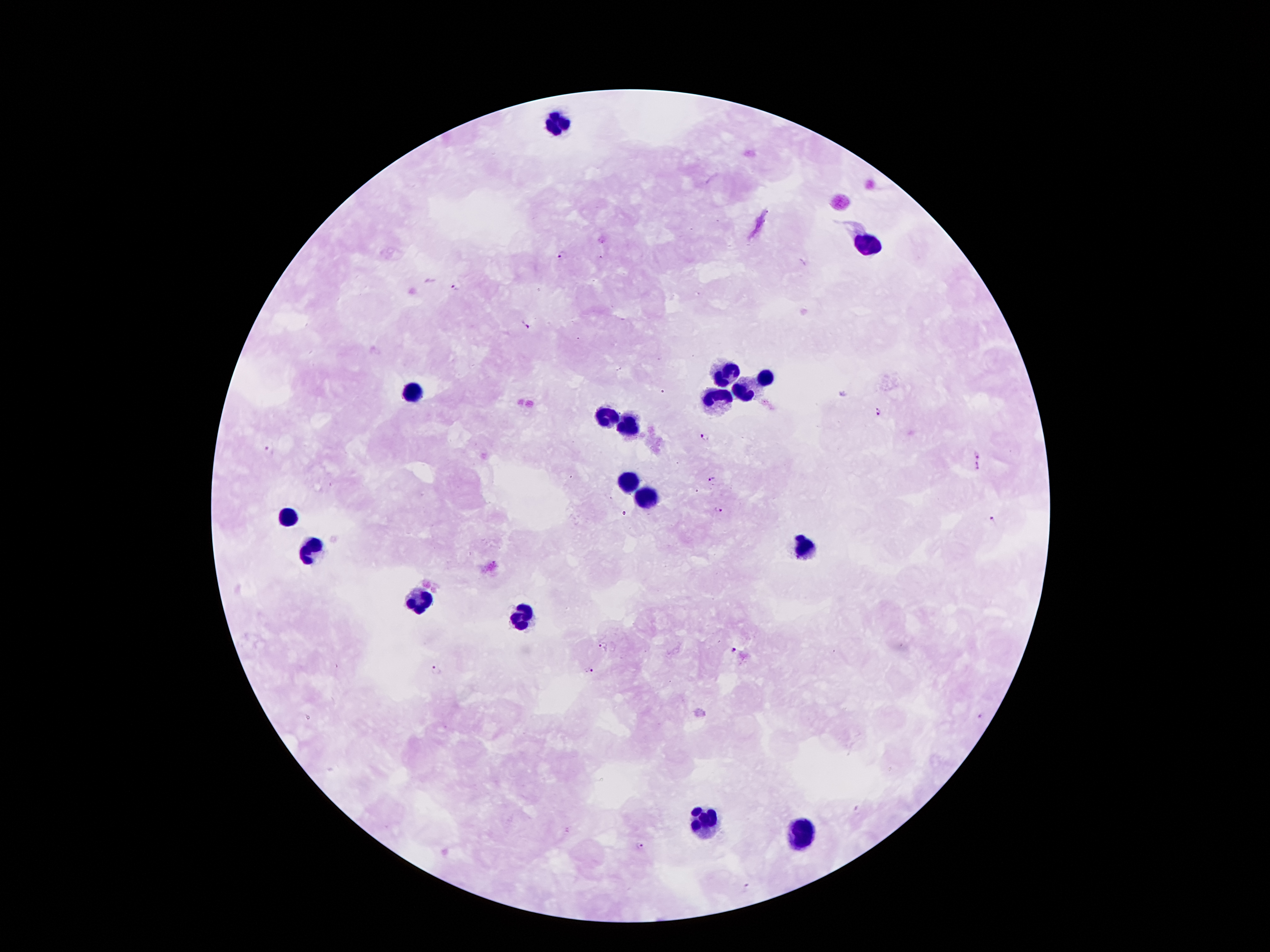

Approximate centers as {x, y} in pixels.
Summary:
  - Leukocyte locations: {559, 123}, {868, 241}, {727, 375}, {764, 379}, {743, 393}, {413, 394}, {719, 401}, {608, 418}, {630, 428}, {628, 479}, {645, 498}, {288, 521}, {311, 549}, {805, 549}, {417, 600}, {522, 619}, {704, 819}, {801, 834}
  - Plasmodium parasite locations: {563, 255}, {456, 287}, {525, 325}, {877, 411}, {704, 435}, {269, 451}, {977, 453}, {977, 468}, {711, 479}, {718, 510}, {994, 522}, {602, 647}, {734, 650}, {589, 670}, {436, 671}, {857, 810}, {641, 848}, {747, 886}
  - Preparation: thick peripheral-blood smear
  - Field of view: one from this slide
  - Stain: Giemsa
  - Magnification: 100x
  - Patient malaria status: positive for Plasmodium falciparum
  - Capture: smartphone camera through the microscope eyepiece
  - Image size: 1270×952 pixels